Assess this cell for malaria.
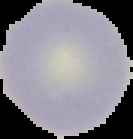
It is uninfected.

Image is 133×139 pixels. The area outside the segmented cell region is set to black. From a thin blood smear.